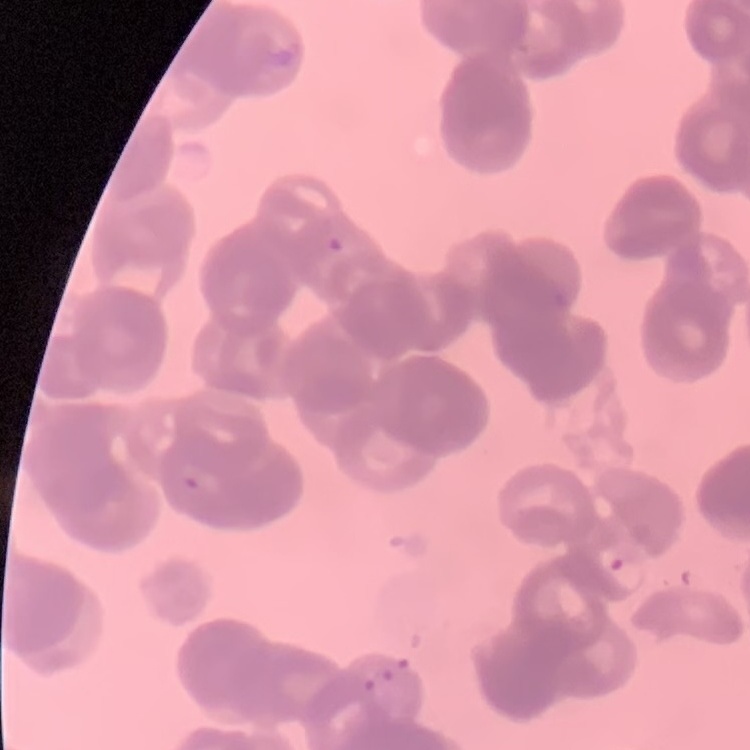
Summary:
  - Erythrocyte morphology: rouleaux formation
  - Image type: square crop of a larger photomicrograph
  - Preparation: thin blood smear
  - Stain: Field's or Giemsa